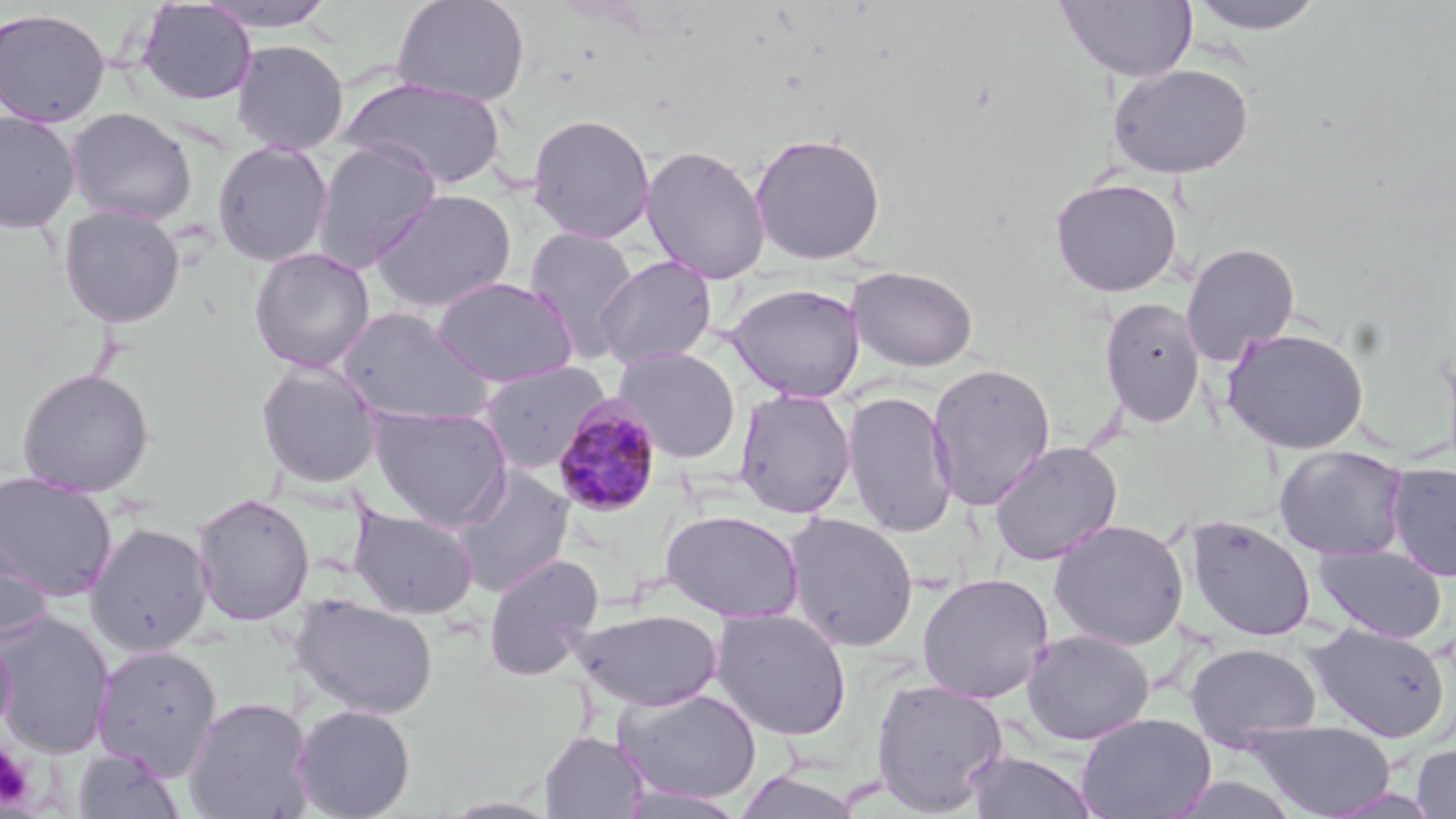
Approximate bounding boxes as (x1,y1)-(x2,y2) corner pairs in pixels. Platelet locations: (0,742)-(35,809). Plasmodium malariae-infected red blood cell locations: (552,394)-(664,516). Uninfected red blood cell locations: (196,0)-(338,32), (392,0)-(530,107), (1054,0)-(1198,82), (1184,0)-(1330,35), (136,1)-(256,106), (0,7)-(111,127), (231,39)-(349,155), (1108,63)-(1254,179), (342,76)-(506,190), (65,107)-(197,226), (0,111)-(81,233), (527,113)-(656,243), (749,132)-(886,265), (212,139)-(333,266), (311,140)-(441,272), (640,145)-(772,284), (1049,177)-(1183,297), (369,188)-(517,313), (58,204)-(185,327), (524,226)-(641,363), (1180,241)-(1301,365), (249,247)-(376,373), (594,255)-(717,370), (847,265)-(979,372), (431,276)-(577,388), (726,283)-(865,402), (1098,296)-(1206,429), (336,308)-(496,427), (1221,327)-(1371,454), (611,346)-(742,463), (256,360)-(383,489), (477,361)-(610,475), (926,362)-(1056,511), (17,368)-(154,497), (733,387)-(857,518), (841,389)-(959,538), (369,404)-(513,530), (988,440)-(1123,566), (1275,445)-(1409,561), (1385,463)-(1456,581), (451,466)-(575,596), (0,473)-(117,601), (191,492)-(314,626), (348,505)-(479,619), (660,509)-(805,623), (783,512)-(920,652), (1184,515)-(1317,642), (1048,518)-(1189,651), (84,522)-(214,656), (0,528)-(53,649), (1312,543)-(1447,643), (483,552)-(604,680), (915,572)-(1055,704), (291,593)-(440,720), (574,608)-(723,711), (711,608)-(852,740), (0,611)-(115,758), (1306,622)-(1451,742), (0,627)-(15,742), (1021,628)-(1155,745), (1184,642)-(1322,751), (92,644)-(222,778), (870,677)-(1010,816), (614,686)-(762,805), (184,696)-(315,819), (291,704)-(416,819), (1076,713)-(1216,819), (1246,718)-(1397,818), (539,730)-(648,818), (1410,741)-(1456,818), (72,747)-(185,819), (964,749)-(1100,818), (732,770)-(865,818), (615,785)-(751,818). Slide-level diagnosis: Plasmodium malariae. One field of a larger specimen. Thin blood film. Light microscopy. Captured at 1000x magnification. Image is 1456×819 pixels. May-Grünwald-Giemsa-stained preparation.